Identify the blood parasite species.
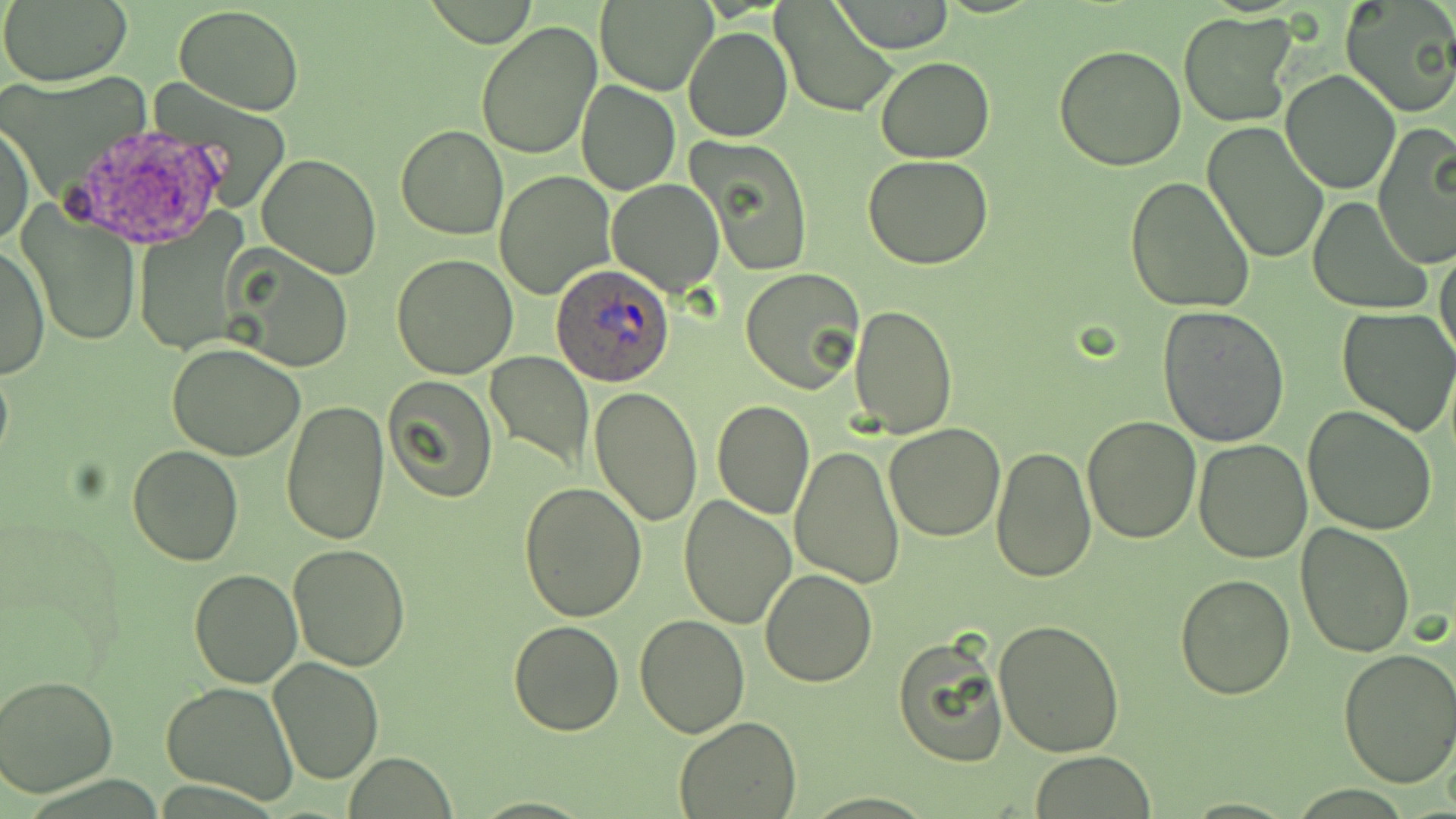

Plasmodium ovale.

uninfected red blood cell locations = approximate bounding boxes as named x1/y1/x2/y2 corners in pixels: (x1=0, y1=0, x2=132, y2=85), (x1=425, y1=0, x2=540, y2=47), (x1=596, y1=0, x2=716, y2=95), (x1=1340, y1=0, x2=1456, y2=118), (x1=771, y1=1, x2=900, y2=119), (x1=833, y1=1, x2=954, y2=53), (x1=174, y1=4, x2=304, y2=114), (x1=1179, y1=10, x2=1298, y2=128), (x1=475, y1=20, x2=603, y2=161), (x1=1303, y1=27, x2=1440, y2=171), (x1=683, y1=28, x2=792, y2=143), (x1=1054, y1=44, x2=1188, y2=171), (x1=876, y1=56, x2=995, y2=163), (x1=1280, y1=69, x2=1400, y2=193), (x1=576, y1=80, x2=679, y2=196), (x1=0, y1=118, x2=35, y2=249), (x1=1202, y1=122, x2=1329, y2=264), (x1=396, y1=125, x2=508, y2=239), (x1=1373, y1=126, x2=1456, y2=269), (x1=689, y1=137, x2=814, y2=277), (x1=256, y1=154, x2=383, y2=278), (x1=864, y1=155, x2=994, y2=271), (x1=495, y1=171, x2=616, y2=299), (x1=1124, y1=178, x2=1256, y2=319), (x1=607, y1=179, x2=723, y2=295), (x1=1308, y1=198, x2=1431, y2=313), (x1=17, y1=206, x2=142, y2=346), (x1=133, y1=222, x2=250, y2=350), (x1=1, y1=241, x2=49, y2=379), (x1=1434, y1=243, x2=1456, y2=366), (x1=223, y1=247, x2=354, y2=372), (x1=392, y1=254, x2=518, y2=379), (x1=740, y1=267, x2=867, y2=396), (x1=848, y1=303, x2=957, y2=438), (x1=1156, y1=305, x2=1289, y2=447), (x1=1337, y1=307, x2=1456, y2=436), (x1=166, y1=342, x2=305, y2=461), (x1=485, y1=352, x2=595, y2=473), (x1=385, y1=374, x2=498, y2=503), (x1=589, y1=386, x2=704, y2=527), (x1=282, y1=398, x2=390, y2=546), (x1=712, y1=400, x2=816, y2=520), (x1=1302, y1=405, x2=1439, y2=535), (x1=1080, y1=413, x2=1201, y2=542), (x1=884, y1=422, x2=1007, y2=542), (x1=1193, y1=439, x2=1312, y2=563), (x1=789, y1=443, x2=905, y2=587), (x1=991, y1=445, x2=1096, y2=583), (x1=127, y1=446, x2=242, y2=565), (x1=517, y1=481, x2=648, y2=622), (x1=678, y1=495, x2=796, y2=629), (x1=1296, y1=521, x2=1415, y2=658), (x1=288, y1=544, x2=411, y2=670), (x1=760, y1=568, x2=877, y2=687), (x1=188, y1=569, x2=302, y2=688), (x1=1173, y1=572, x2=1294, y2=700), (x1=634, y1=613, x2=749, y2=738), (x1=508, y1=619, x2=627, y2=736), (x1=993, y1=619, x2=1127, y2=756), (x1=892, y1=631, x2=1009, y2=768), (x1=1338, y1=648, x2=1456, y2=787), (x1=267, y1=657, x2=384, y2=784), (x1=0, y1=675, x2=118, y2=797), (x1=160, y1=681, x2=299, y2=806), (x1=673, y1=715, x2=801, y2=817), (x1=346, y1=752, x2=458, y2=818), (x1=1028, y1=752, x2=1157, y2=818)
image size = 1456×819 pixels
field of view = one of a larger specimen
Plasmodium ovale-infected red blood cell locations = approximate bounding boxes as named x1/y1/x2/y2 corners in pixels: (x1=551, y1=263, x2=676, y2=386)
preparation = thin blood film
magnification = 1000x
stain = May-Grünwald-Giemsa
modality = light microscopy